Outline each blood parasite and name the species.
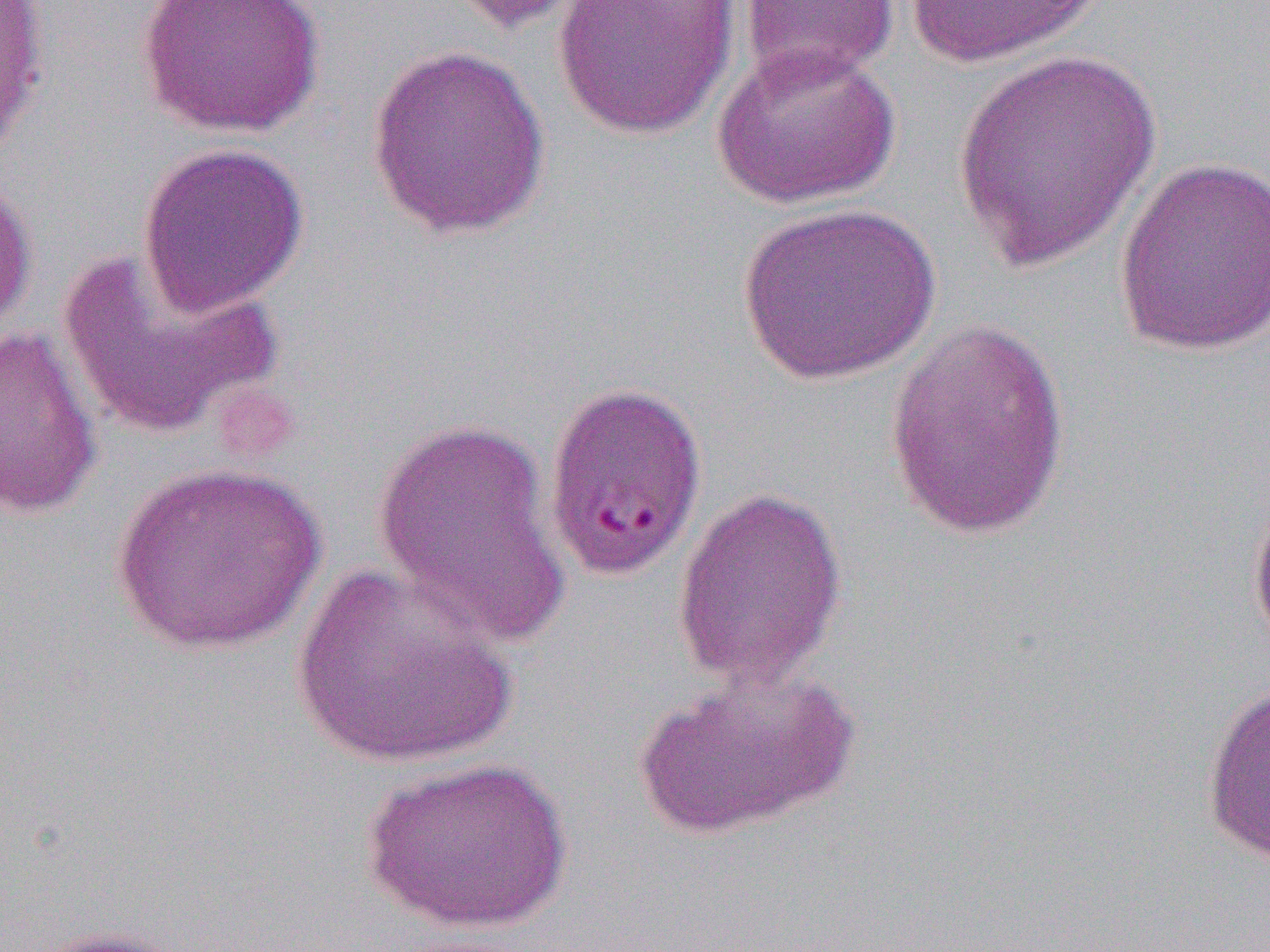

Approximate bounding boxes as [x1, y1, x2, y2] in pixels.
Plasmodium falciparum-infected red blood cells: [542, 378, 710, 581].
No Plasmodium ovale, Plasmodium malariae, Plasmodium vivax, Babesia divergens, or Trypanosoma brucei observed.

slide_level_diagnosis: Plasmodium falciparum
preparation: thin blood film
uninfected_red_blood_cell_locations: 'approximate bounding boxes as [x1, y1, x2, y2] in pixels: [0, 0, 51, 166], [136, 0, 326, 139], [443, 0, 596, 35], [552, 0, 740, 140], [902, 0, 1112, 69], [738, 1, 899, 86], [365, 41, 552, 240], [711, 41, 902, 209], [951, 47, 1164, 276], [136, 142, 310, 317], [1112, 155, 1270, 359], [0, 171, 37, 337], [735, 201, 940, 386], [58, 248, 283, 439], [885, 320, 1071, 539], [0, 324, 104, 521], [371, 415, 571, 652], [109, 461, 326, 655], [672, 485, 848, 689], [1247, 490, 1270, 655], [290, 560, 518, 771], [634, 661, 858, 841], [1200, 679, 1270, 869], [359, 753, 575, 935], [20, 924, 194, 952]'
field_of_view: one of a larger specimen
magnification: 1000x
modality: light microscopy
image_size: 1270×952 pixels